State which cell type is depicted.
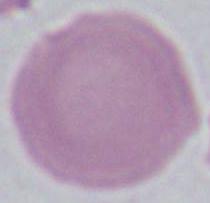
This is an erythrocyte.

modality = micrograph
magnification = 1000x